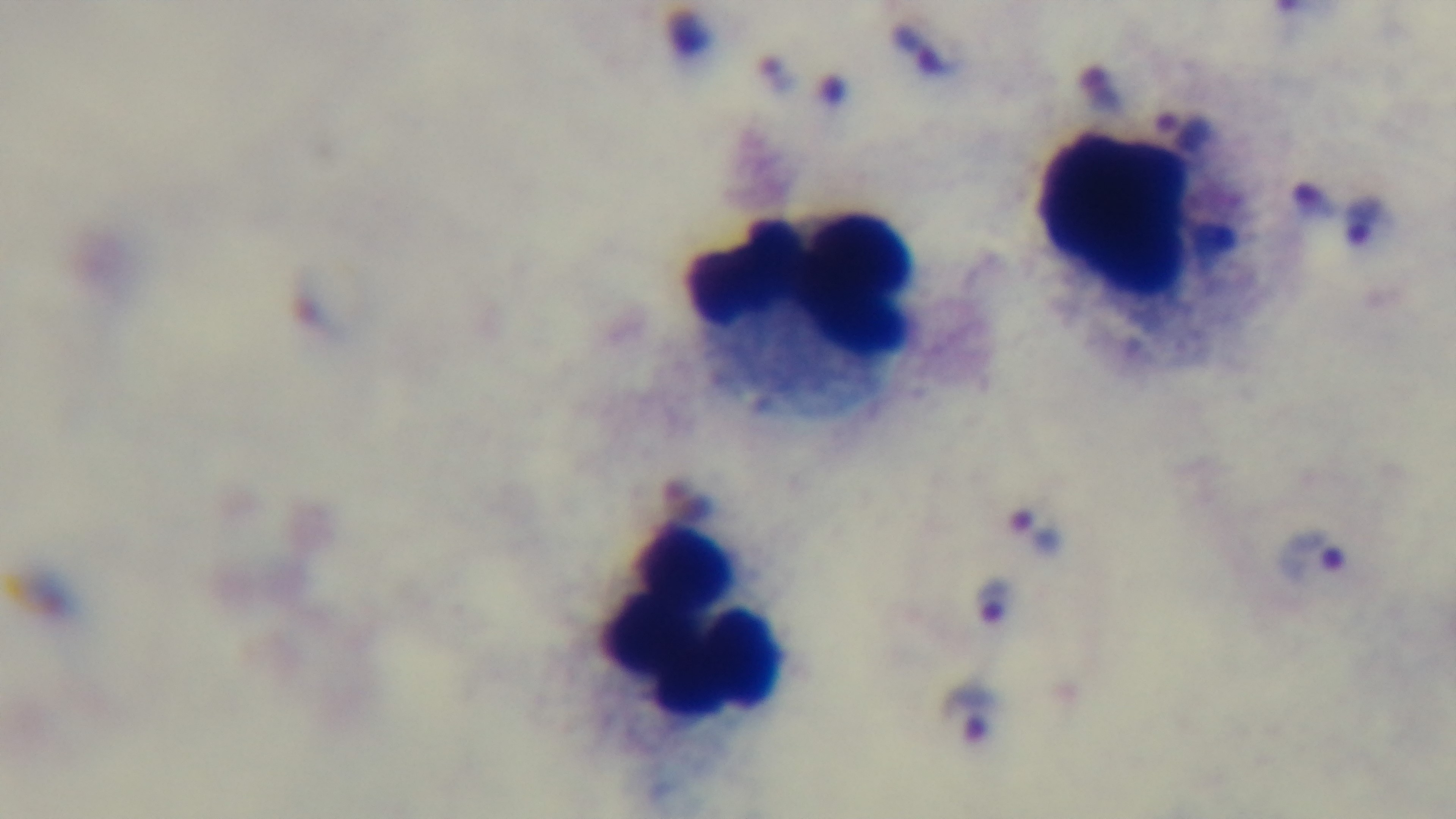
Summary:
  - Capture: mounted 4K digital camera
  - Modality: light microscopy
  - Preparation: thick
  - Malaria status: positive
  - Field of view: single
  - Objective: 100x oil immersion
  - Stain: Giemsa